Report the malaria status of this cell.
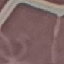
Uninfected.

image_type: automatically extracted cell patch, resized to 64 × 64 pixels
stain: Giemsa
capture: smartphone camera at the microscope eyepiece
preparation: thin blood film